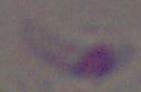 Toxoplasma gondii is seen. Photomicrograph. Captured at 1000x magnification.